Report the malaria status of this cell.
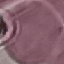
It is uninfected.

Summary:
  - Capture: smartphone camera at the microscope eyepiece
  - Stain: Giemsa
  - Image type: cell patch, automatically extracted from a larger field of view and resized to 64 × 64 pixels
  - Preparation: thin smear